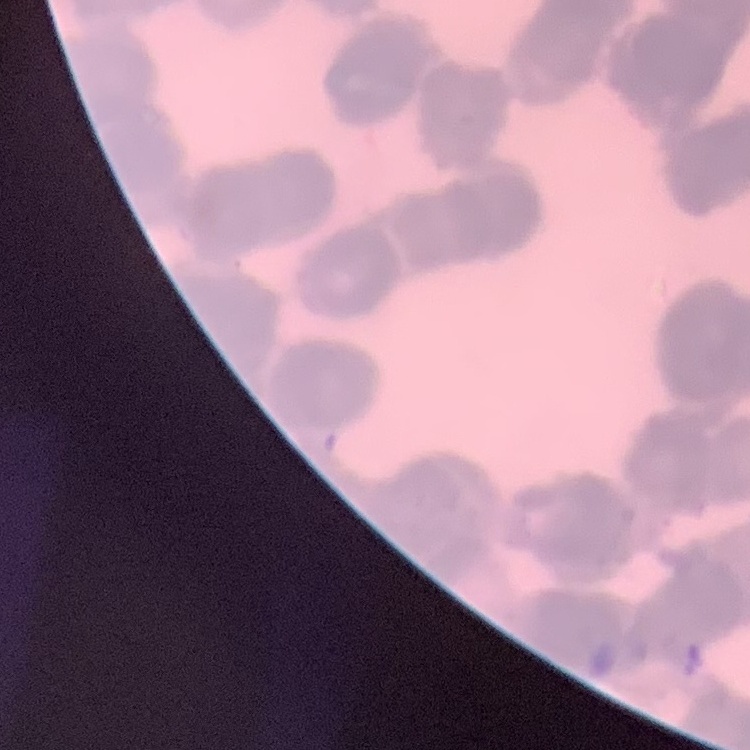 The red blood cells exhibit rouleaux formation. Thin blood film. Field's or Giemsa stain. Square crop of a larger photomicrograph.